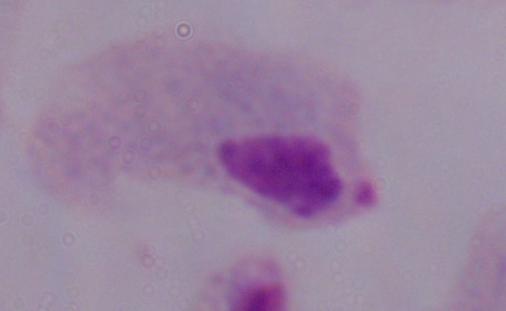

Summary:
  - Modality: micrograph
  - Magnification: 1000x
  - Identification: trichomonad